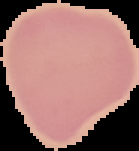

malaria status = uninfected
image size = 139×151 pixels
image type = segmented cell region with the area outside set to black
preparation = thin blood film